Outline each uninfected red blood cell.
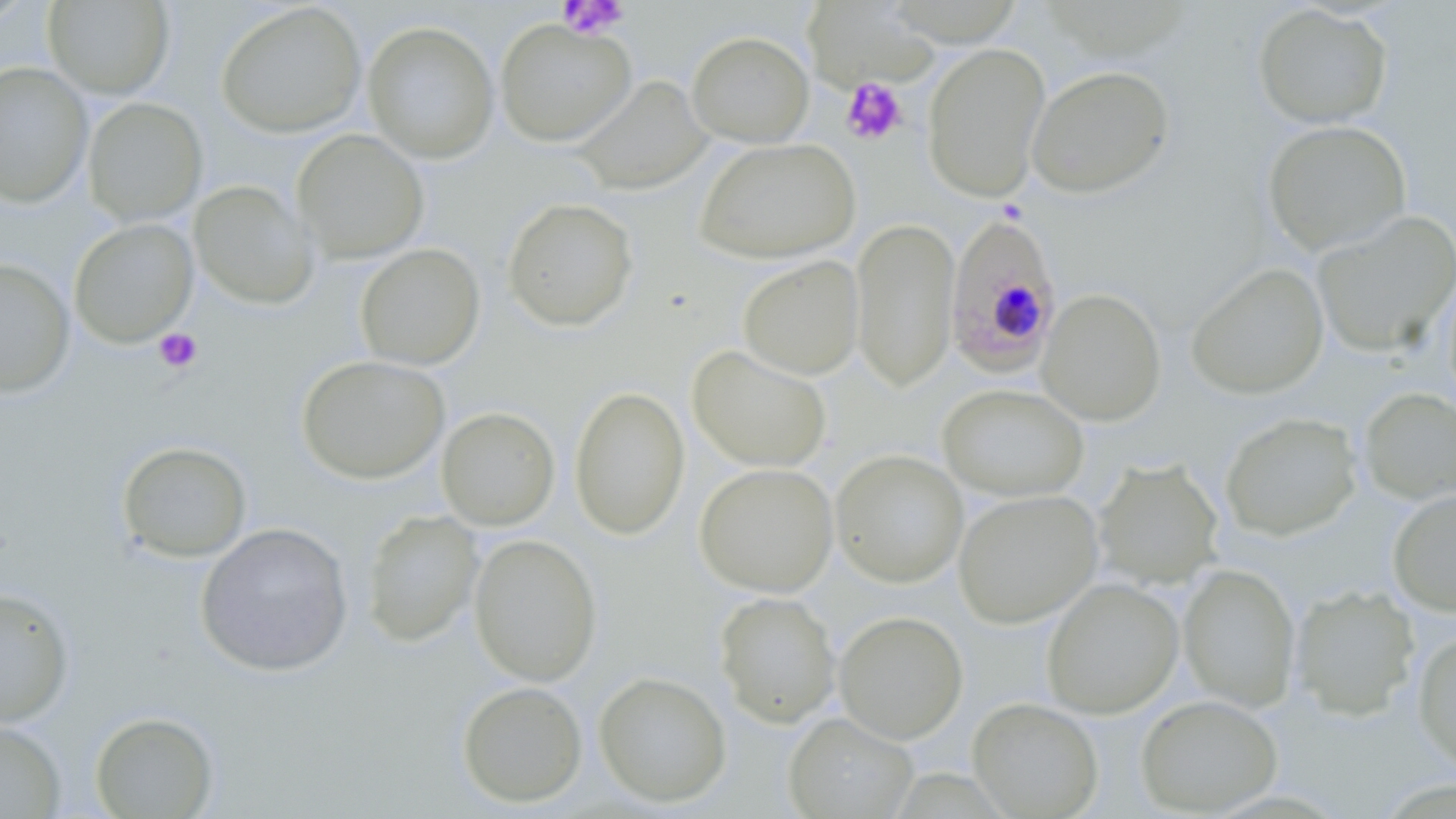

Approximate bounding boxes as (x1, y1, x2, y2) in pixels.
Uninfected red blood cells: (0, 1, 35, 31), (43, 1, 175, 99), (801, 1, 936, 90), (216, 2, 366, 138), (1253, 3, 1393, 129), (495, 19, 636, 147), (362, 21, 500, 164), (687, 30, 814, 147), (922, 42, 1051, 202), (0, 62, 93, 207), (1027, 65, 1175, 198), (573, 75, 713, 195), (82, 97, 208, 226), (1262, 119, 1412, 256), (292, 129, 429, 263), (695, 137, 860, 265), (188, 180, 319, 310), (502, 197, 639, 332), (1311, 210, 1456, 360), (851, 216, 960, 392), (69, 218, 199, 348), (355, 243, 486, 371), (737, 256, 864, 380), (0, 258, 75, 397), (1186, 262, 1329, 400), (1037, 288, 1167, 426), (688, 344, 832, 472), (296, 354, 450, 484), (937, 383, 1089, 502), (569, 385, 690, 540), (1358, 388, 1456, 507), (436, 406, 560, 531), (1219, 411, 1363, 541), (116, 440, 252, 563), (830, 449, 969, 588), (1093, 458, 1224, 590), (694, 462, 839, 597), (1387, 488, 1456, 616), (953, 489, 1103, 628), (361, 510, 484, 647), (195, 522, 354, 677), (469, 533, 602, 686), (1178, 564, 1300, 712), (1041, 578, 1184, 718), (1290, 585, 1420, 721), (0, 586, 75, 727), (714, 591, 841, 728), (834, 610, 968, 743), (1412, 629, 1456, 776), (593, 671, 732, 807), (456, 680, 588, 807), (1135, 694, 1283, 816), (967, 697, 1104, 819), (89, 710, 219, 818), (783, 711, 918, 818), (0, 720, 66, 818).

Plasmodium falciparum-infected red blood cell locations: (943, 212, 1064, 378). Platelet locations: (557, 0, 629, 39), (840, 77, 908, 146), (153, 328, 202, 373). Slide-level diagnosis: Plasmodium falciparum. One field of a larger specimen. 1000x magnification. Thin blood film. May-Grünwald-Giemsa stain. Light microscopy. Image is 1456×819 pixels.